Assess this cell for malaria.
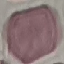

It is uninfected.

Photographed with a smartphone camera at the microscope eyepiece. Automatically extracted cell patch, resized to 64 × 64 pixels. Thin smear of blood. Giemsa stain.